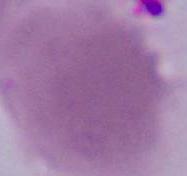

Captured at 1000x magnification. Photomicrograph. An erythrocyte is seen.